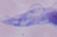
modality = micrograph
identification = trypanosome
magnification = 1000x